Assess this cell for malaria.
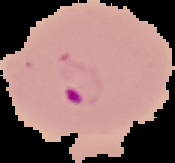

Parasitized.

Summary:
  - Image size: 175×163 pixels
  - Image type: segmented cell region with the area outside set to black
  - Preparation: thin blood film